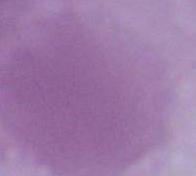

Summary:
  - Magnification: 1000x
  - Modality: micrograph
  - Identification: red blood cell